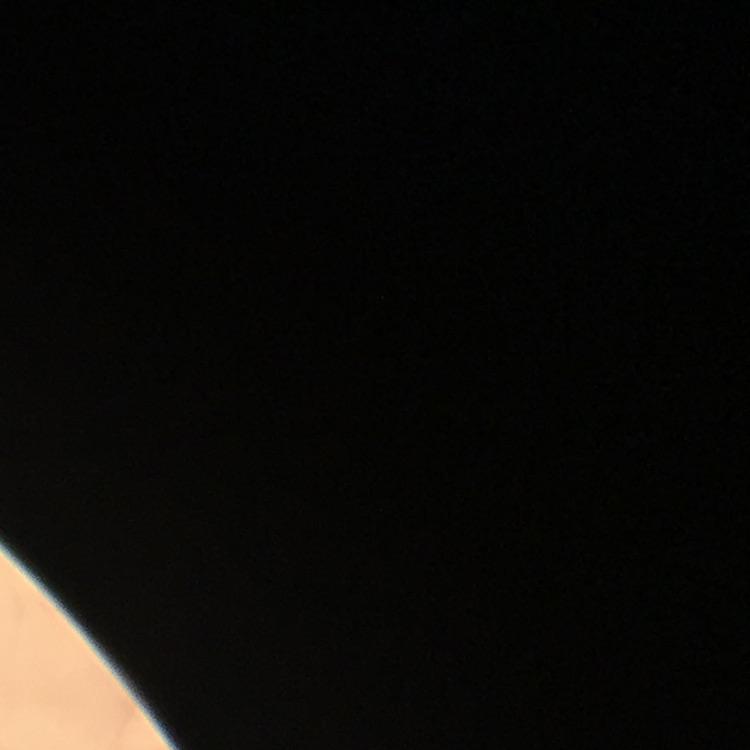 Thick blood film. 100x magnification. Photographed with a smartphone mounted on the microscope. Giemsa stain. Image is 750×750 pixels. Immersion oil was used. A crop from one field of view. From a malaria diagnostic workup.